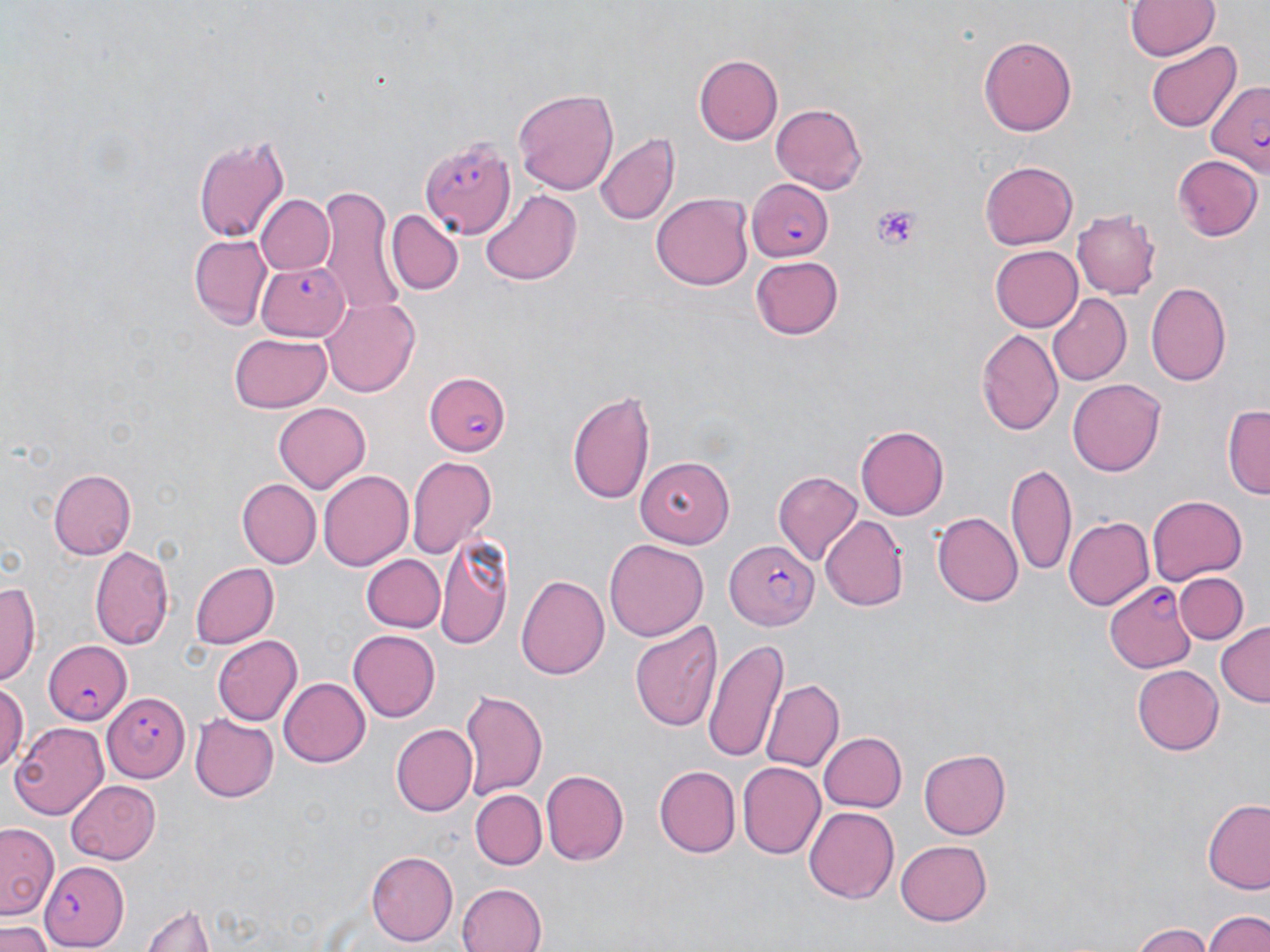

Summary:
  - Coordinate format: approximate bounding boxes as (x1, y1, x2, y2) in pixels
  - Uninfected red blood cell locations: (1124, 2, 1219, 62), (979, 33, 1076, 137), (1145, 40, 1240, 132), (694, 55, 783, 145), (512, 86, 619, 194), (769, 103, 868, 195), (594, 132, 680, 226), (193, 134, 291, 245), (1171, 153, 1261, 241), (980, 163, 1077, 249), (316, 187, 403, 313), (480, 189, 580, 285), (651, 193, 753, 291), (255, 194, 334, 277), (1072, 207, 1163, 297), (386, 209, 462, 295), (189, 233, 272, 328), (991, 245, 1084, 331), (749, 256, 843, 340), (1146, 279, 1231, 385), (1044, 294, 1130, 386), (321, 297, 421, 397), (976, 328, 1063, 435), (231, 331, 331, 411), (1067, 379, 1167, 476), (567, 390, 656, 505), (273, 401, 371, 491), (1224, 404, 1270, 500), (855, 426, 949, 519), (405, 455, 495, 557), (635, 457, 738, 545), (1007, 463, 1078, 579), (49, 467, 136, 560), (320, 470, 413, 570), (773, 471, 862, 565), (235, 477, 319, 567), (1147, 494, 1248, 585), (932, 511, 1022, 606), (1064, 515, 1153, 611), (820, 516, 908, 611), (435, 532, 513, 650), (604, 539, 709, 642), (90, 544, 175, 652), (361, 554, 446, 633), (190, 563, 278, 648), (516, 572, 609, 683), (1175, 572, 1249, 645), (0, 580, 40, 688), (630, 618, 723, 734), (1216, 622, 1270, 707), (347, 629, 440, 721), (211, 635, 303, 724), (705, 637, 785, 762), (1132, 665, 1225, 755), (278, 676, 370, 767), (760, 680, 843, 773), (0, 681, 26, 774), (458, 686, 547, 800), (190, 713, 279, 802), (11, 722, 108, 816), (391, 723, 478, 817), (818, 732, 908, 812), (919, 749, 1010, 839), (738, 763, 826, 858), (654, 766, 741, 857), (541, 770, 627, 867), (65, 779, 162, 862), (472, 790, 545, 869), (1202, 799, 1270, 893), (803, 806, 898, 903), (0, 821, 60, 920), (896, 839, 992, 924), (366, 848, 457, 945), (455, 882, 548, 952), (138, 903, 216, 952), (1203, 909, 1270, 952), (0, 922, 54, 952), (1128, 922, 1211, 952)
  - Plasmodium falciparum-infected red blood cell locations: (1204, 80, 1270, 172), (421, 136, 516, 238), (746, 176, 832, 261), (256, 262, 351, 341), (422, 369, 513, 457), (723, 541, 817, 628), (1106, 581, 1195, 672), (41, 638, 132, 723), (106, 691, 188, 782), (39, 859, 130, 952)
  - Platelet locations: (868, 203, 921, 254)
  - Slide-level diagnosis: Plasmodium falciparum
  - Image size: 1270×952 pixels
  - Magnification: 1000x
  - Field of view: one of a larger specimen
  - Preparation: thin blood film
  - Stain: May-Grünwald-Giemsa
  - Modality: optical microscopy